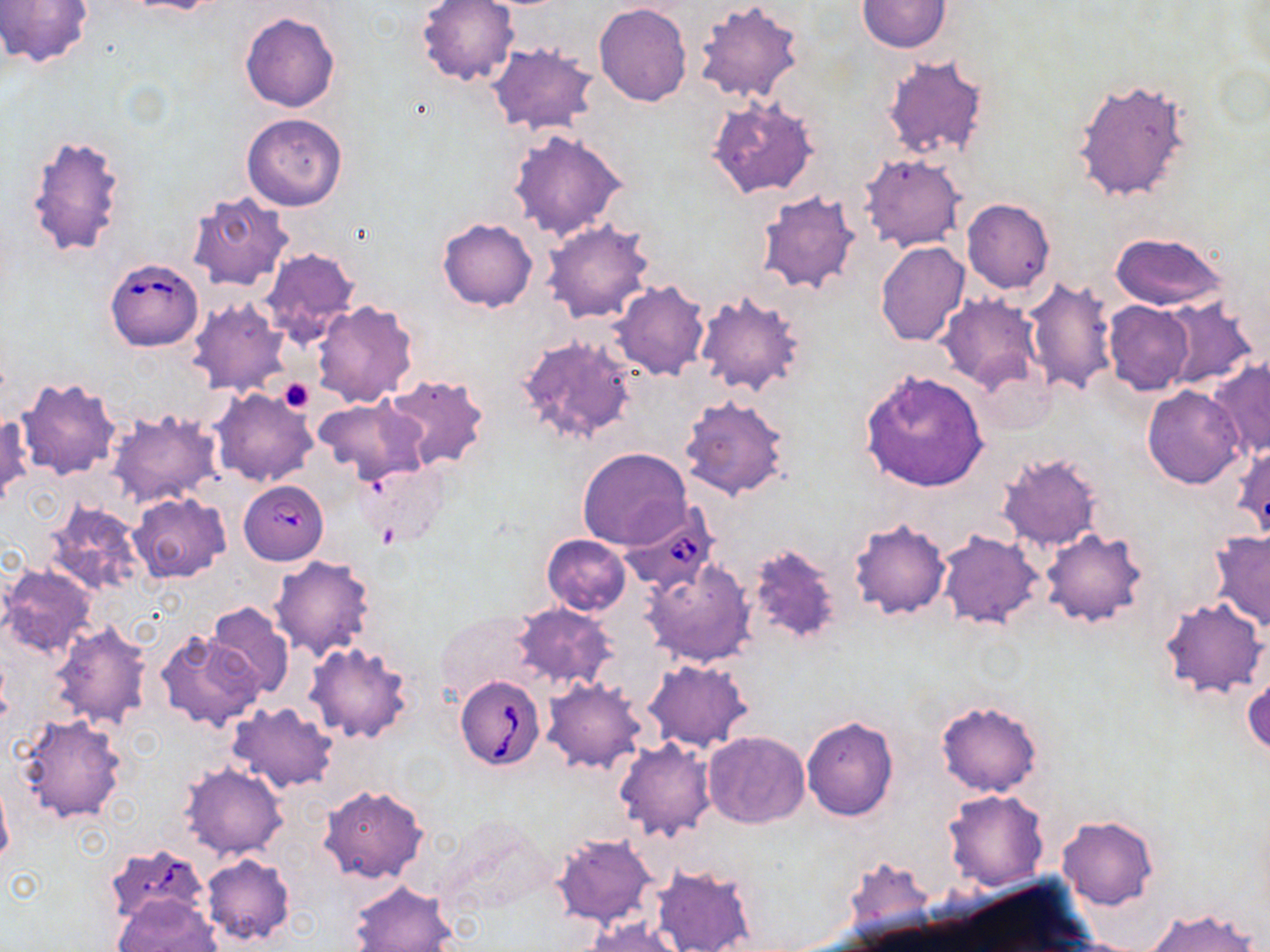

{
  "slide_level_diagnosis": "Babesia divergens",
  "stain": "May-Grünwald-Giemsa",
  "babesia_divergens_infected_red_blood_cell_locations": "approximate bounding boxes as (x1, y1, x2, y2) in pixels: (105, 257, 203, 352), (239, 481, 329, 565), (619, 504, 717, 596), (453, 673, 546, 771), (104, 844, 211, 928)",
  "uninfected_red_blood_cell_locations": "approximate bounding boxes as (x1, y1, x2, y2) in pixels: (0, 0, 93, 68), (115, 0, 227, 14), (856, 0, 953, 53), (416, 1, 519, 88), (693, 1, 805, 102), (594, 3, 692, 107), (239, 11, 340, 113), (487, 43, 602, 136), (881, 54, 991, 163), (1072, 76, 1193, 204), (707, 96, 819, 200), (242, 113, 348, 211), (508, 128, 629, 240), (24, 131, 128, 260), (860, 153, 965, 251), (754, 189, 862, 296), (187, 192, 292, 292), (961, 198, 1055, 294), (437, 217, 537, 312), (541, 218, 654, 324), (1109, 231, 1228, 313), (875, 241, 970, 346), (258, 246, 360, 346), (1021, 276, 1119, 398), (610, 280, 710, 380), (695, 291, 808, 396), (936, 293, 1043, 396), (1159, 297, 1261, 389), (187, 299, 292, 396), (310, 300, 420, 407), (1103, 300, 1195, 395), (514, 333, 638, 445), (1207, 360, 1269, 458), (859, 369, 989, 493), (381, 373, 491, 471), (17, 376, 121, 481), (1143, 385, 1245, 488), (211, 389, 316, 488), (679, 395, 791, 500), (313, 396, 429, 484), (107, 408, 224, 508), (1, 412, 32, 507), (1231, 441, 1270, 543), (578, 447, 692, 552), (996, 452, 1104, 553), (357, 462, 450, 549), (129, 494, 230, 582), (44, 501, 147, 597), (848, 518, 950, 619), (937, 529, 1045, 630), (1040, 529, 1148, 628), (1208, 530, 1270, 632), (542, 535, 631, 616), (745, 540, 845, 647), (269, 556, 377, 661), (642, 561, 754, 667), (0, 564, 97, 658), (1159, 597, 1267, 698), (205, 602, 295, 699), (510, 602, 618, 692), (435, 611, 541, 709), (48, 619, 155, 733), (155, 629, 264, 732), (304, 641, 414, 744), (643, 659, 751, 752), (1242, 664, 1269, 759), (542, 678, 648, 772), (934, 698, 1044, 797), (227, 702, 338, 794), (15, 713, 128, 824), (801, 715, 900, 821), (703, 732, 811, 829), (614, 739, 715, 842), (178, 763, 288, 860), (0, 771, 13, 872), (318, 783, 430, 884), (943, 789, 1049, 890), (1057, 815, 1158, 910), (551, 832, 658, 929), (201, 852, 296, 948), (842, 856, 937, 945), (650, 861, 758, 952), (348, 879, 458, 952), (113, 894, 220, 952), (1144, 907, 1259, 952), (585, 918, 684, 952)",
  "magnification": "1000x",
  "image_size": "1270×952 pixels",
  "preparation": "thin blood smear",
  "field_of_view": "one of a larger specimen",
  "modality": "light microscopy",
  "platelet_locations": "approximate bounding boxes as (x1, y1, x2, y2) in pixels: (280, 377, 315, 414)"
}